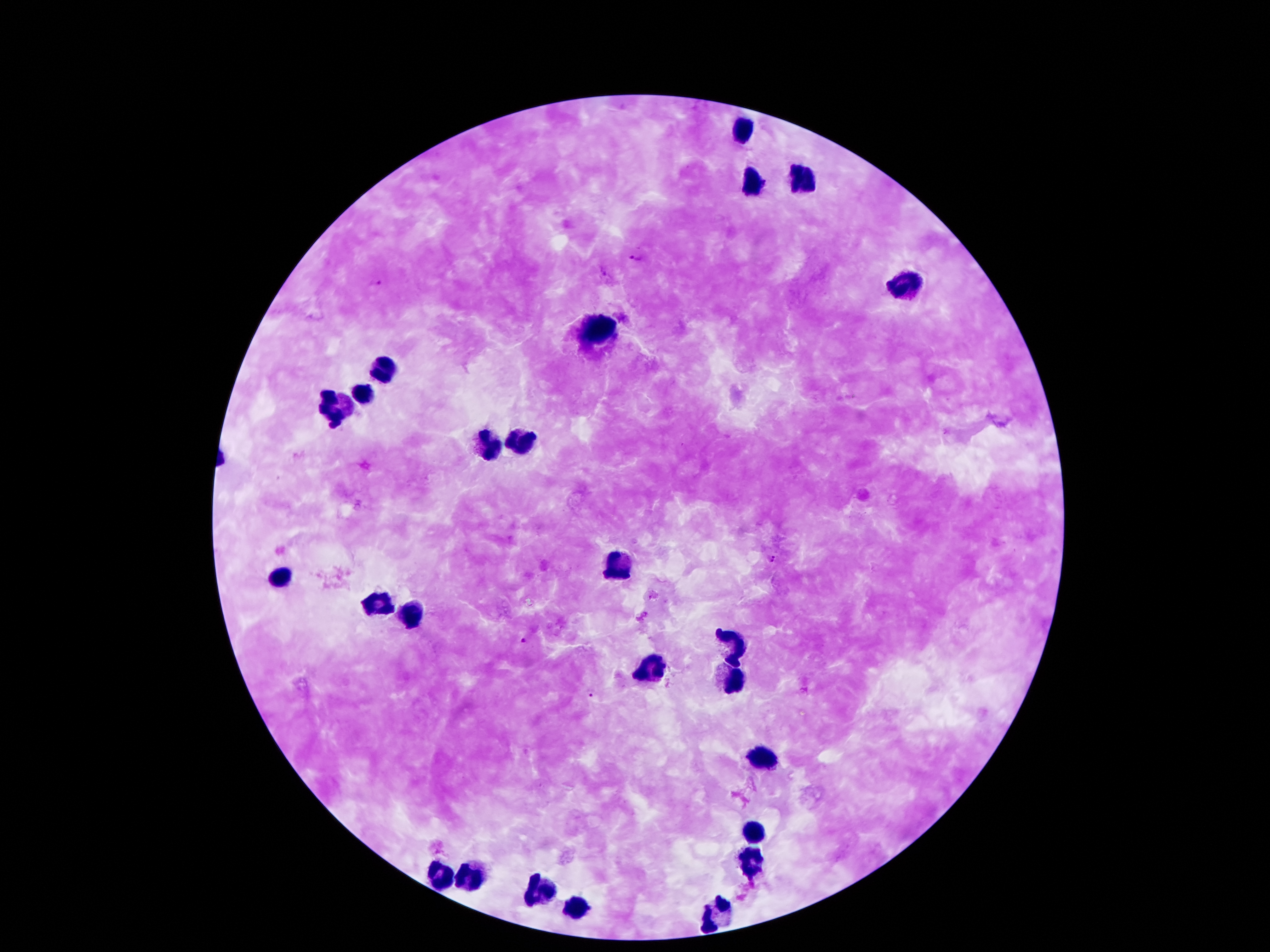
coordinate format = approximate centers as (x, y) in pixels
leukocyte locations = (741, 133), (754, 184), (796, 184), (905, 281), (596, 330), (381, 362), (363, 392), (334, 414), (521, 444), (494, 446), (610, 569), (282, 575), (373, 602), (405, 616), (734, 639), (650, 669), (734, 683), (759, 762), (754, 830), (751, 865), (445, 874), (470, 874), (539, 891), (576, 907), (717, 913)
Plasmodium parasite locations = (636, 258), (606, 273), (376, 282), (623, 318), (772, 558), (524, 642), (592, 694)
field of view = single
magnification = 100x
image size = 1270×952 pixels
capture = smartphone through the microscope eyepiece
patient malaria status = infected with Plasmodium falciparum
preparation = thick blood smear
stain = Giemsa